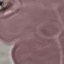
result: no malaria parasites seen
image_type: automatically extracted cell patch, resized to 64 × 64 pixels
capture: smartphone through the microscope eyepiece
preparation: thin blood smear
stain: Giemsa